Classify this cell by malaria status.
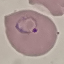
It is parasitized.

Summary:
  - Capture: smartphone camera at the microscope eyepiece
  - Image type: cell patch, automatically extracted from a larger field of view and resized to 64 × 64 pixels
  - Stain: Giemsa
  - Preparation: thin blood smear